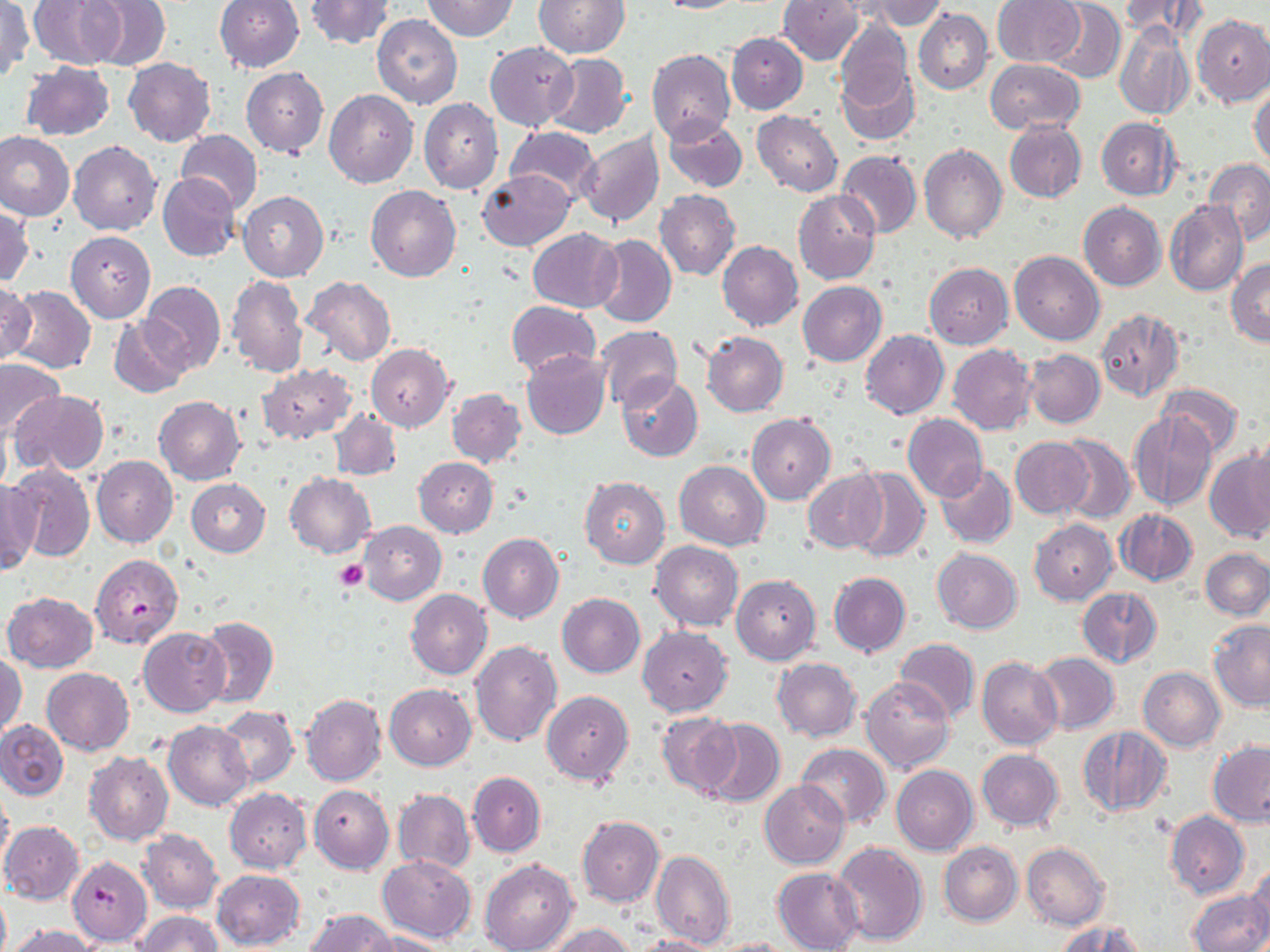

slide-level diagnosis = Plasmodium falciparum
uninfected red blood cell locations = approximate bounding boxes as (x1, y1, x2, y2) in pixels: (30, 0, 124, 69), (85, 0, 170, 69), (215, 0, 304, 73), (423, 0, 518, 40), (534, 0, 629, 57), (655, 0, 748, 14), (858, 0, 944, 30), (1120, 0, 1206, 41), (305, 1, 393, 50), (778, 1, 862, 65), (992, 1, 1084, 66), (1046, 1, 1126, 84), (0, 2, 32, 80), (913, 8, 993, 94), (371, 14, 463, 109), (1193, 14, 1270, 106), (835, 19, 912, 109), (1114, 21, 1194, 121), (726, 33, 807, 114), (485, 41, 577, 131), (647, 50, 736, 146), (543, 52, 632, 138), (124, 57, 216, 146), (986, 59, 1084, 134), (21, 61, 114, 140), (835, 62, 920, 146), (241, 68, 328, 158), (1250, 83, 1270, 168), (324, 89, 418, 188), (418, 98, 503, 194), (752, 110, 843, 196), (662, 116, 747, 192), (1097, 116, 1182, 200), (1004, 121, 1085, 203), (505, 127, 600, 208), (176, 130, 263, 214), (578, 131, 664, 229), (0, 132, 74, 222), (69, 139, 162, 236), (920, 146, 1007, 244), (837, 151, 921, 239), (1203, 158, 1270, 245), (477, 170, 574, 250), (159, 175, 240, 260), (367, 186, 461, 281), (793, 189, 880, 285), (654, 190, 741, 279), (239, 191, 328, 281), (1165, 200, 1248, 297), (1079, 202, 1165, 291), (1, 206, 33, 287), (528, 228, 621, 311), (66, 230, 155, 322), (591, 234, 677, 328), (718, 241, 803, 331), (1009, 251, 1104, 345), (1227, 259, 1270, 347), (932, 260, 1018, 433), (924, 262, 1013, 349), (226, 275, 308, 377), (302, 275, 397, 367), (140, 280, 226, 373), (0, 281, 37, 367), (798, 281, 886, 366), (6, 285, 96, 374), (506, 300, 599, 377), (1095, 307, 1184, 401), (110, 318, 190, 398), (595, 325, 683, 412), (860, 330, 950, 419), (701, 331, 788, 416), (948, 343, 1036, 435), (366, 344, 454, 431), (1023, 349, 1104, 428), (521, 350, 611, 439), (0, 359, 65, 438), (256, 363, 357, 445), (617, 374, 704, 461), (1159, 383, 1244, 457), (447, 387, 526, 467), (11, 390, 108, 475), (155, 397, 246, 484), (329, 410, 402, 479), (1129, 411, 1219, 511), (748, 412, 835, 504), (903, 414, 988, 502), (1053, 435, 1134, 525), (1245, 436, 1270, 518), (1010, 438, 1093, 518), (1205, 448, 1270, 542), (91, 456, 178, 547), (415, 457, 497, 537), (674, 460, 770, 550), (937, 463, 1017, 549), (5, 465, 95, 561), (848, 468, 928, 563), (802, 470, 887, 554), (284, 473, 376, 558), (581, 477, 670, 568), (186, 479, 271, 557), (0, 480, 40, 575), (1115, 509, 1197, 586), (1030, 520, 1116, 603), (358, 521, 445, 604), (477, 533, 563, 623), (650, 541, 743, 631), (932, 548, 1022, 634), (1201, 548, 1270, 618), (828, 572, 910, 656), (731, 574, 821, 664), (1076, 587, 1163, 669), (406, 589, 492, 679), (3, 591, 99, 672), (558, 593, 645, 677), (199, 616, 278, 709), (1208, 619, 1270, 710), (638, 625, 733, 716), (140, 627, 229, 715), (894, 638, 980, 722), (470, 641, 561, 746), (1031, 652, 1119, 735), (0, 653, 27, 737), (977, 656, 1062, 750), (773, 658, 862, 741), (41, 666, 134, 755), (1138, 668, 1224, 751), (861, 677, 955, 775), (385, 683, 477, 770), (541, 690, 634, 786), (300, 693, 385, 787), (217, 706, 298, 788), (657, 713, 740, 798), (698, 717, 786, 808), (0, 720, 68, 799), (163, 720, 253, 810), (1078, 726, 1171, 819), (1208, 741, 1270, 827), (796, 743, 892, 828), (977, 749, 1064, 831), (85, 751, 173, 845), (891, 765, 978, 854), (468, 771, 545, 856), (760, 780, 849, 867), (0, 782, 13, 875), (309, 784, 393, 873), (224, 788, 311, 872), (393, 789, 474, 873), (1165, 811, 1250, 898), (577, 815, 664, 907), (1, 821, 84, 904), (138, 829, 221, 912), (831, 841, 928, 947), (939, 841, 1022, 927), (1021, 842, 1111, 930), (651, 850, 734, 950), (376, 855, 476, 943), (480, 858, 578, 952), (1247, 865, 1270, 946), (773, 867, 864, 952), (211, 869, 304, 949), (1188, 889, 1270, 952), (0, 890, 10, 952), (304, 908, 395, 951), (133, 911, 224, 951), (1059, 921, 1148, 952), (546, 923, 637, 952), (7, 924, 100, 952), (363, 930, 451, 952), (632, 935, 721, 952), (709, 937, 799, 952)
preparation = thin blood smear
image size = 1270×952 pixels
modality = light microscopy
stain = May-Grünwald-Giemsa
magnification = 1000x
platelet locations = approximate bounding boxes as (x1, y1, x2, y2) in pixels: (334, 560, 368, 592)
field of view = single
Plasmodium falciparum-infected red blood cell locations = approximate bounding boxes as (x1, y1, x2, y2) in pixels: (90, 555, 183, 648), (67, 855, 153, 947)